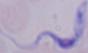
Summary:
  - Magnification: 1000x
  - Modality: photomicrograph
  - Identification: trypanosome